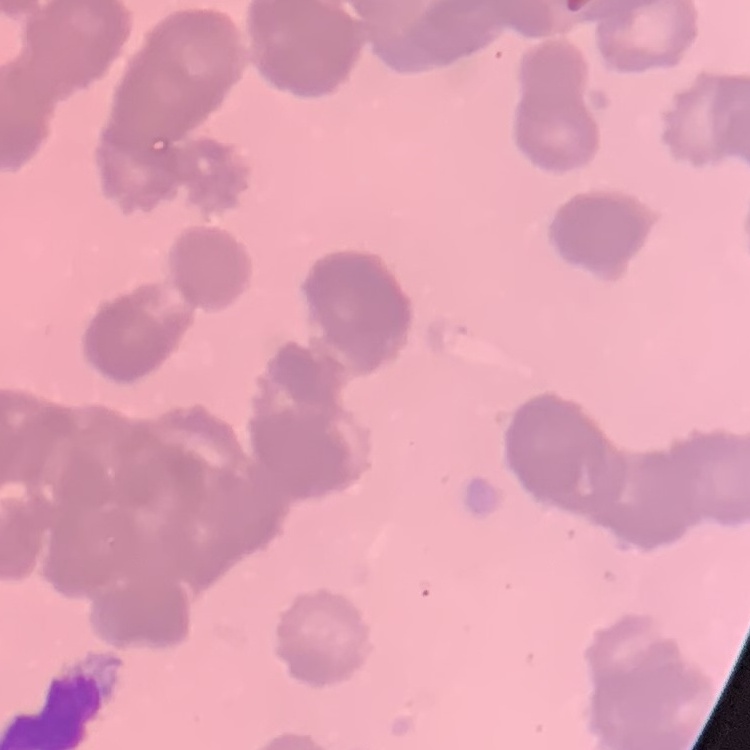

Summary:
  - Erythrocyte morphology: rouleaux formation
  - Preparation: thin blood film
  - Image type: one tile cut from a larger photomicrograph
  - Stain: Field's or Giemsa